Classify this cell by malaria status.
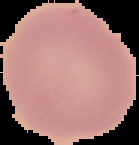
It is uninfected.

Summary:
  - Image size: 139×145 pixels
  - Image type: segmented cell region with the area outside set to black
  - Preparation: thin blood film